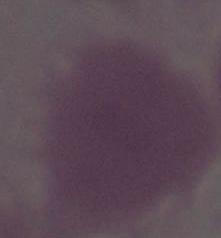

identification = red blood cell
modality = photomicrograph
magnification = 1000x